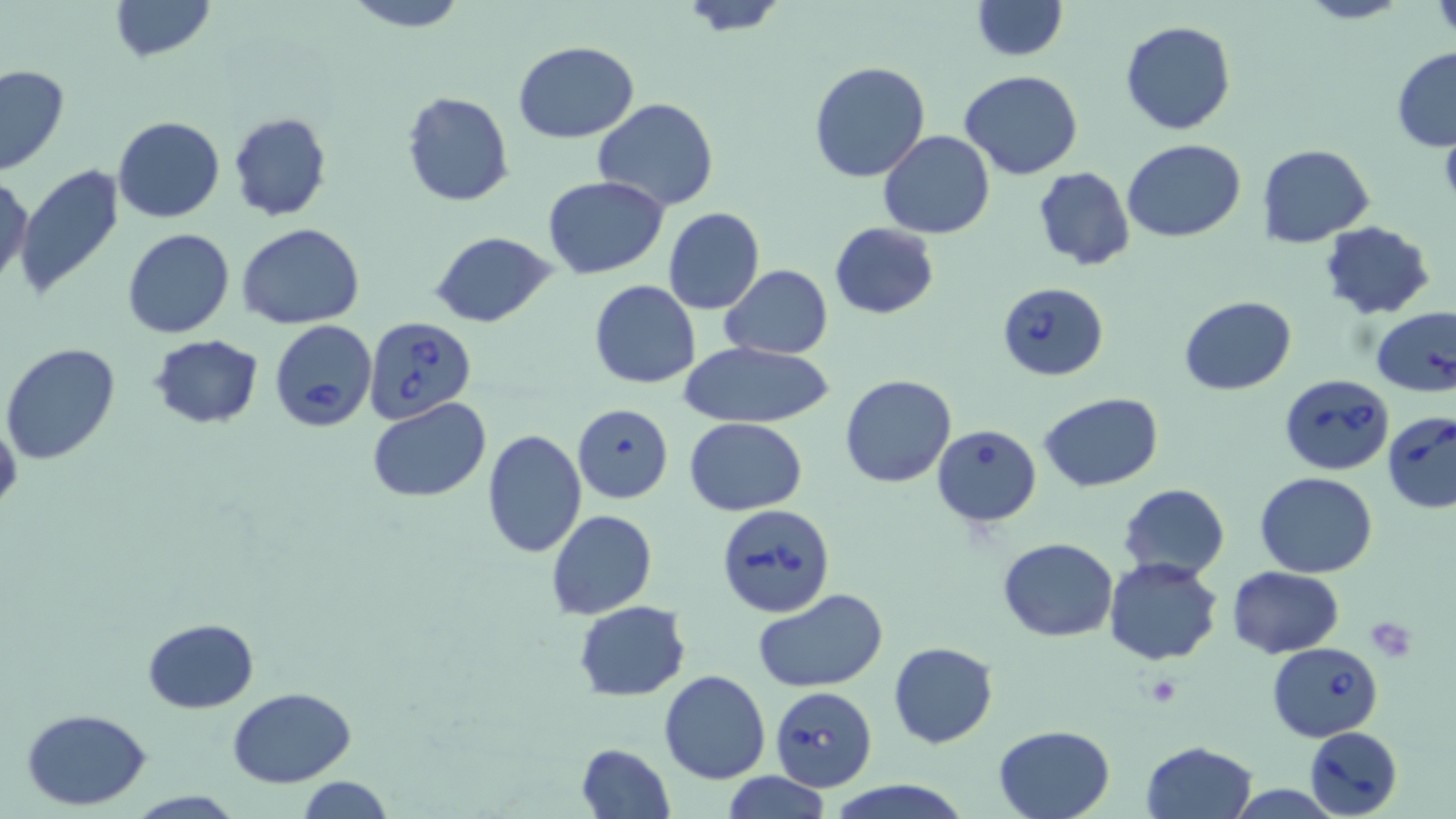
Approximate bounding boxes as (x1,y1)-(x2,y2) corner pairs in pixels. Uninfected red blood cell locations: (110,0)-(214,62), (341,0)-(469,31), (971,0)-(1067,59), (1297,0)-(1407,24), (1430,0)-(1456,40), (676,1)-(791,37), (1119,20)-(1236,135), (513,39)-(640,143), (1391,47)-(1456,152), (808,62)-(931,183), (0,65)-(70,176), (959,70)-(1085,180), (401,91)-(516,207), (592,98)-(721,212), (227,111)-(331,222), (112,117)-(225,223), (879,129)-(995,240), (1122,140)-(1245,241), (1258,144)-(1375,247), (13,165)-(126,301), (1032,165)-(1134,272), (1,173)-(33,290), (543,176)-(667,278), (663,206)-(765,314), (1320,221)-(1436,318), (829,222)-(939,319), (237,224)-(366,328), (122,229)-(234,338), (430,231)-(556,328), (719,266)-(834,359), (589,280)-(701,388), (1178,295)-(1297,396), (1371,306)-(1456,399), (149,334)-(264,429), (679,341)-(837,429), (1,342)-(122,465), (841,374)-(957,489), (1040,393)-(1164,490), (368,399)-(491,503), (572,402)-(674,503), (0,415)-(22,516), (684,417)-(807,515), (481,429)-(586,559), (1257,472)-(1377,578), (1118,482)-(1231,581), (546,509)-(658,621), (998,538)-(1120,640), (1103,559)-(1223,666), (1228,566)-(1343,658), (754,588)-(888,692), (573,601)-(691,700), (143,617)-(258,712), (888,642)-(996,749), (659,670)-(771,784), (227,685)-(357,786), (22,709)-(152,810), (992,724)-(1116,819), (1140,741)-(1257,819), (577,742)-(674,818), (721,772)-(833,819), (296,777)-(397,817), (825,779)-(970,819), (124,789)-(245,818). Platelet locations: (1365,619)-(1416,659), (1144,675)-(1180,704). Babesia divergens-infected red blood cell locations: (997,283)-(1109,381), (365,316)-(477,423), (269,320)-(377,432), (1279,374)-(1395,475), (1383,412)-(1456,514), (932,425)-(1042,528), (715,502)-(834,620), (1268,641)-(1383,742), (770,686)-(877,792), (1305,725)-(1403,818). Slide-level diagnosis: Babesia divergens. May-Grünwald-Giemsa stain. Image is 1456×819 pixels. Thin blood film. Captured at 1000x magnification. One field of a larger specimen. Optical microscopy.